Assess this cell for malaria.
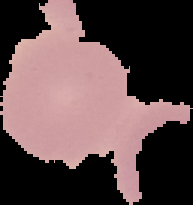

It is uninfected.

image type = segmented cell region on a black background
preparation = thin blood smear
image size = 193×205 pixels